Identify the parasite.
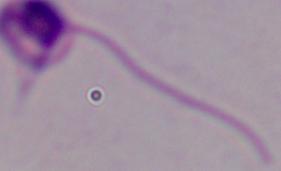

This is Leishmania.

Summary:
  - Magnification: 1000x
  - Modality: photomicrograph